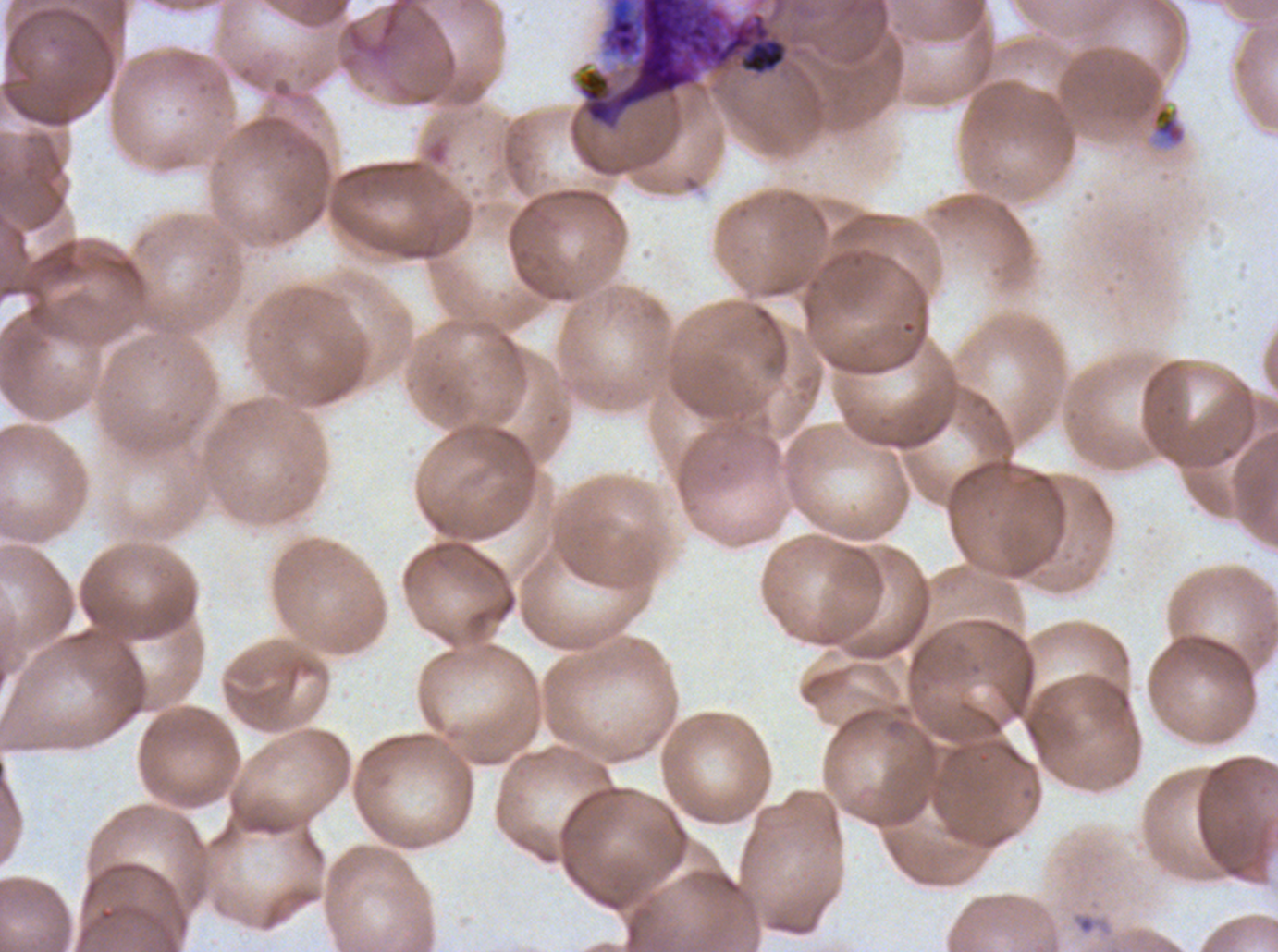

Approximate bounding boxes as {x1, y1, x2, y2} in pixels.
Summary:
  - Debris locations: {576, 0, 789, 129}, {1151, 103, 1186, 147}
  - Field of view: one sub-image of a larger composite
  - Image size: 1278×952 pixels
  - Specimen: ex-vivo P. falciparum culture from a patient in The Gambia, grown for 24 to 48 hours
  - Preparation: thin blood smear
  - Stain: Giemsa